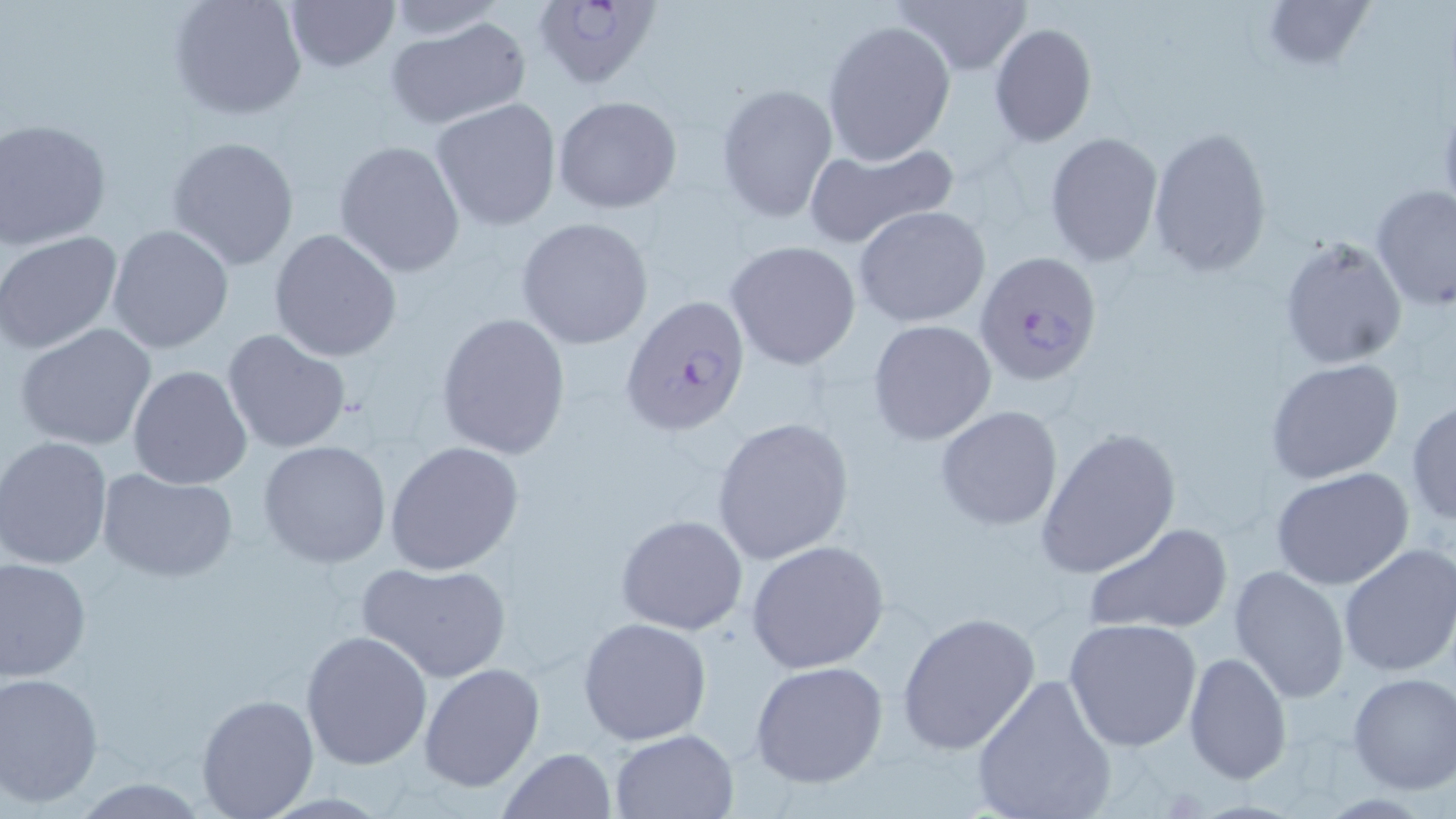

Summary:
  - Coordinate format: approximate bounding boxes as named x1/y1/x2/y2 corners in pixels
  - Uninfected red blood cell locations: (x1=282, y1=0, x2=400, y2=75), (x1=894, y1=0, x2=1034, y2=76), (x1=1261, y1=0, x2=1377, y2=70), (x1=168, y1=1, x2=306, y2=121), (x1=381, y1=1, x2=511, y2=40), (x1=385, y1=15, x2=532, y2=131), (x1=822, y1=19, x2=956, y2=165), (x1=989, y1=22, x2=1097, y2=148), (x1=715, y1=84, x2=838, y2=223), (x1=550, y1=94, x2=684, y2=214), (x1=431, y1=99, x2=562, y2=231), (x1=1, y1=120, x2=112, y2=249), (x1=1147, y1=127, x2=1272, y2=277), (x1=1045, y1=131, x2=1163, y2=265), (x1=167, y1=135, x2=300, y2=270), (x1=332, y1=139, x2=467, y2=278), (x1=803, y1=141, x2=959, y2=249), (x1=1370, y1=185, x2=1456, y2=313), (x1=853, y1=205, x2=990, y2=327), (x1=516, y1=217, x2=655, y2=350), (x1=107, y1=225, x2=233, y2=353), (x1=268, y1=228, x2=402, y2=362), (x1=0, y1=229, x2=124, y2=356), (x1=1278, y1=234, x2=1408, y2=367), (x1=724, y1=239, x2=863, y2=370), (x1=434, y1=312, x2=571, y2=459), (x1=868, y1=319, x2=997, y2=446), (x1=14, y1=322, x2=158, y2=451), (x1=222, y1=330, x2=351, y2=455), (x1=1265, y1=358, x2=1403, y2=482), (x1=128, y1=365, x2=253, y2=489), (x1=1406, y1=398, x2=1456, y2=525), (x1=935, y1=406, x2=1063, y2=532), (x1=711, y1=415, x2=855, y2=566), (x1=1034, y1=426, x2=1180, y2=581), (x1=0, y1=437, x2=113, y2=569), (x1=258, y1=440, x2=391, y2=569), (x1=385, y1=441, x2=525, y2=577), (x1=1271, y1=467, x2=1415, y2=591), (x1=98, y1=469, x2=238, y2=582), (x1=614, y1=514, x2=750, y2=636), (x1=1082, y1=521, x2=1230, y2=637), (x1=746, y1=540, x2=890, y2=674), (x1=1338, y1=542, x2=1456, y2=678), (x1=0, y1=556, x2=92, y2=682), (x1=355, y1=559, x2=513, y2=684), (x1=1227, y1=566, x2=1349, y2=705), (x1=896, y1=611, x2=1041, y2=755), (x1=577, y1=616, x2=712, y2=744), (x1=1063, y1=619, x2=1204, y2=752), (x1=299, y1=628, x2=433, y2=770), (x1=1182, y1=651, x2=1293, y2=785), (x1=418, y1=661, x2=545, y2=792), (x1=750, y1=661, x2=891, y2=789), (x1=1, y1=672, x2=104, y2=807), (x1=1347, y1=672, x2=1456, y2=794), (x1=969, y1=673, x2=1118, y2=819), (x1=196, y1=693, x2=319, y2=818), (x1=610, y1=729, x2=738, y2=817), (x1=499, y1=748, x2=617, y2=819)
  - Plasmodium falciparum-infected red blood cell locations: (x1=538, y1=0, x2=666, y2=88), (x1=974, y1=252, x2=1103, y2=387), (x1=620, y1=293, x2=751, y2=437)
  - Slide-level diagnosis: Plasmodium falciparum
  - Magnification: 1000x
  - Image size: 1456×819 pixels
  - Stain: May-Grünwald-Giemsa
  - Field of view: single
  - Modality: optical microscopy
  - Preparation: thin blood film